Give a bounding box for every parasitised red blood cell.
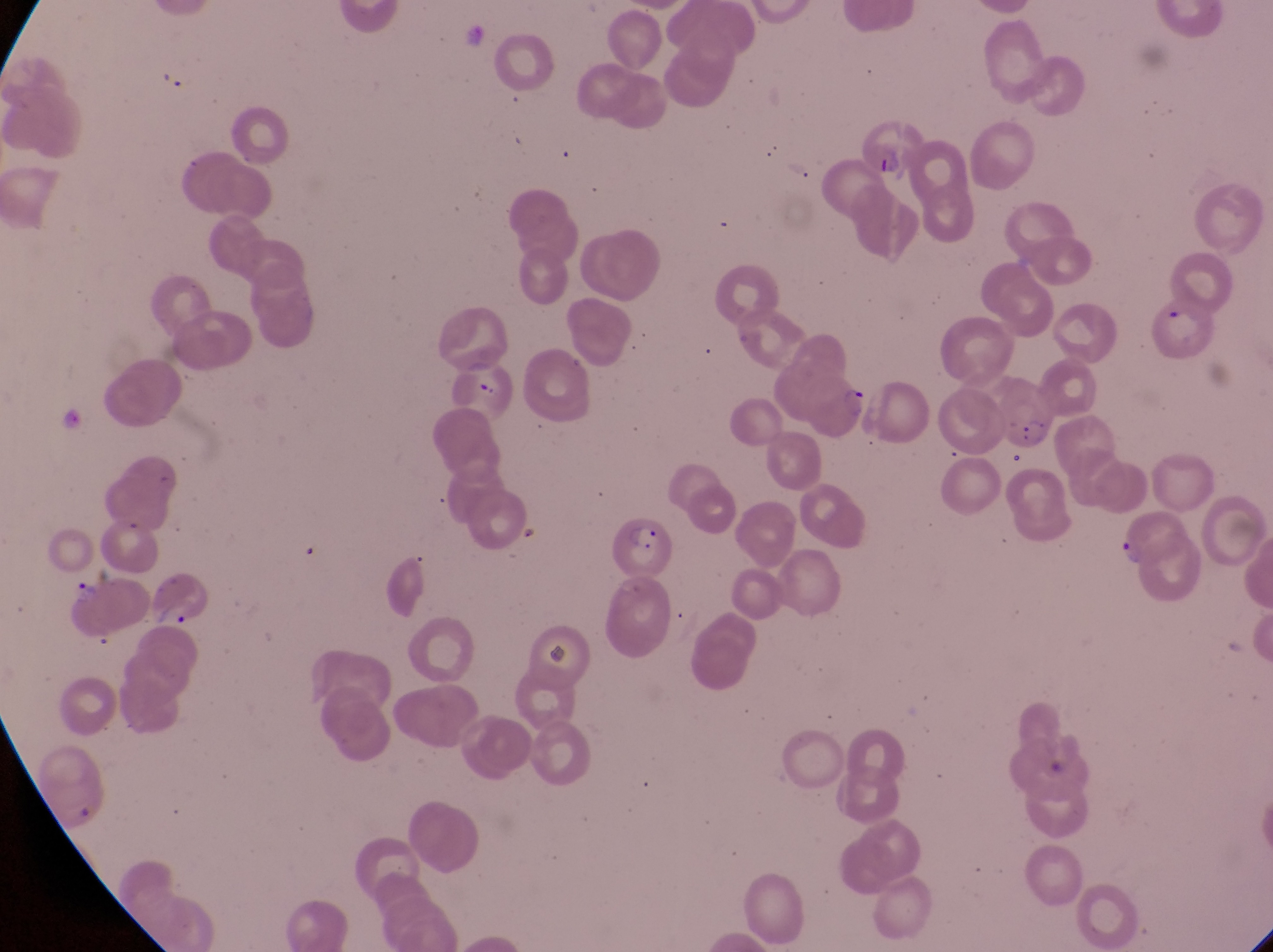
Approximate bounding boxes as {left, top, right, bottom} in pixels.
Parasitised red blood cells: {860, 113, 922, 173}, {1153, 297, 1222, 374}, {808, 369, 868, 443}, {996, 374, 1056, 452}, {607, 504, 676, 576}.

Summary:
  - Trophozoite locations: {63, 574, 100, 614}, {157, 594, 190, 636}
  - Artifact (platelet-like body, stain precipitate, or debris) locations: {459, 352, 514, 424}
  - Magnification: 1000x
  - Field of view: single
  - Image size: 1273×952 pixels
  - Country: Uganda
  - Preparation: thin blood film
  - Capture: smartphone photograph through the eyepiece of an Olympus CX-23 microscope